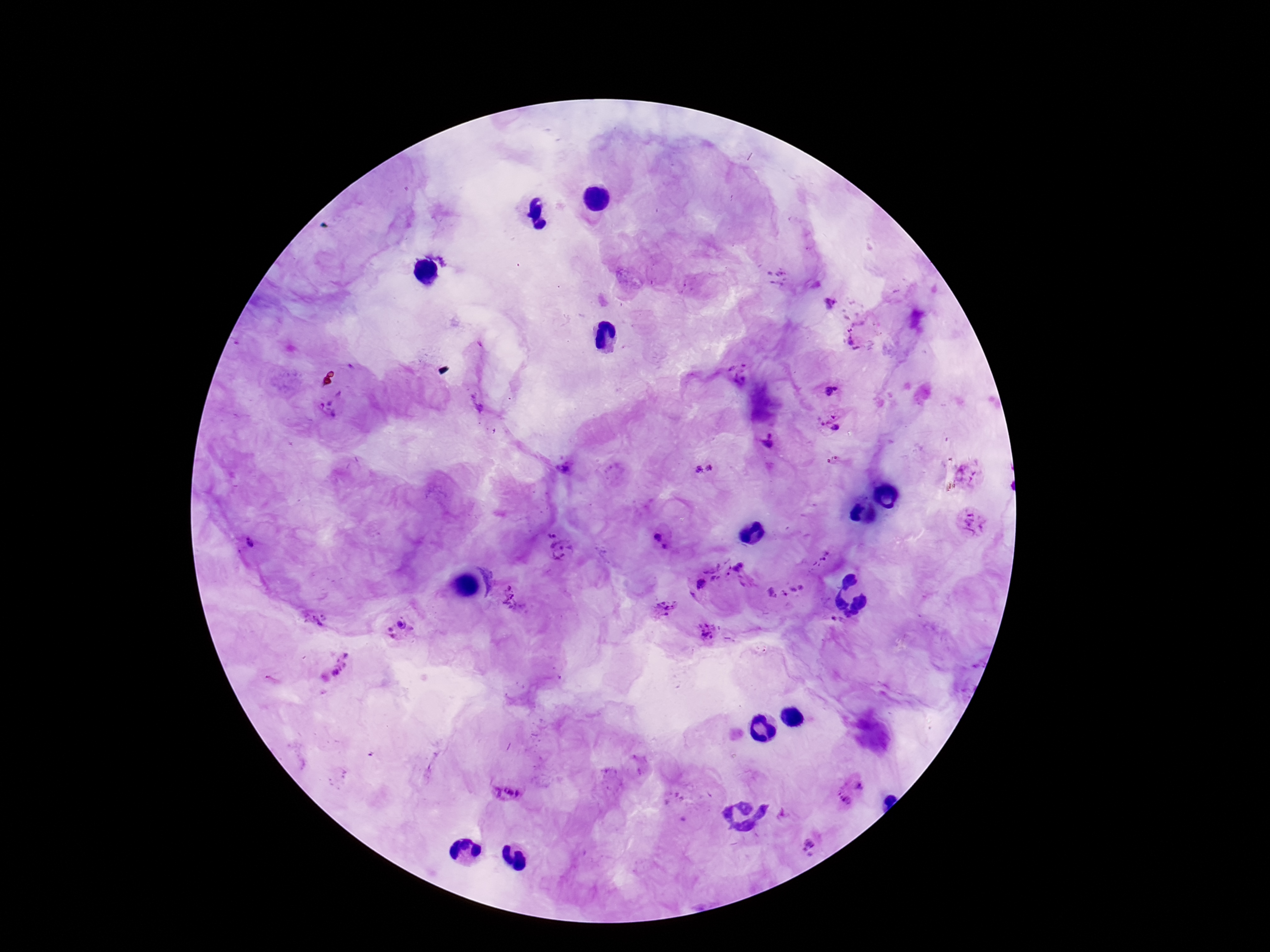 Approximate centers as [x, y] in pixels. Plasmodium parasite locations: [831, 304], [854, 337], [832, 390], [329, 407], [830, 422], [767, 442], [709, 467], [566, 468], [697, 469], [970, 474], [971, 522], [550, 533], [660, 539], [249, 543], [562, 551], [820, 560], [718, 571], [744, 573], [698, 586], [784, 592], [512, 600], [666, 607], [401, 628], [708, 633], [335, 666], [506, 786], [852, 791], [809, 845]. Patient malaria status: infected. Single field of view. Thick blood smear. Giemsa-stained preparation. 100x magnification. Image is 1270×952 pixels. Photographed through the microscope eyepiece with a smartphone camera.